Classify this cell by malaria status.
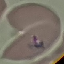

Parasitized.

image type = automatically extracted cell patch, resized to 64 × 64 pixels
preparation = thin blood film
capture = smartphone through the microscope eyepiece
stain = Giemsa